Report the malaria status of this cell.
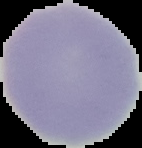
It is uninfected.

Summary:
  - Image type: segmented cell region on a black background
  - Image size: 142×148 pixels
  - Preparation: thin blood smear